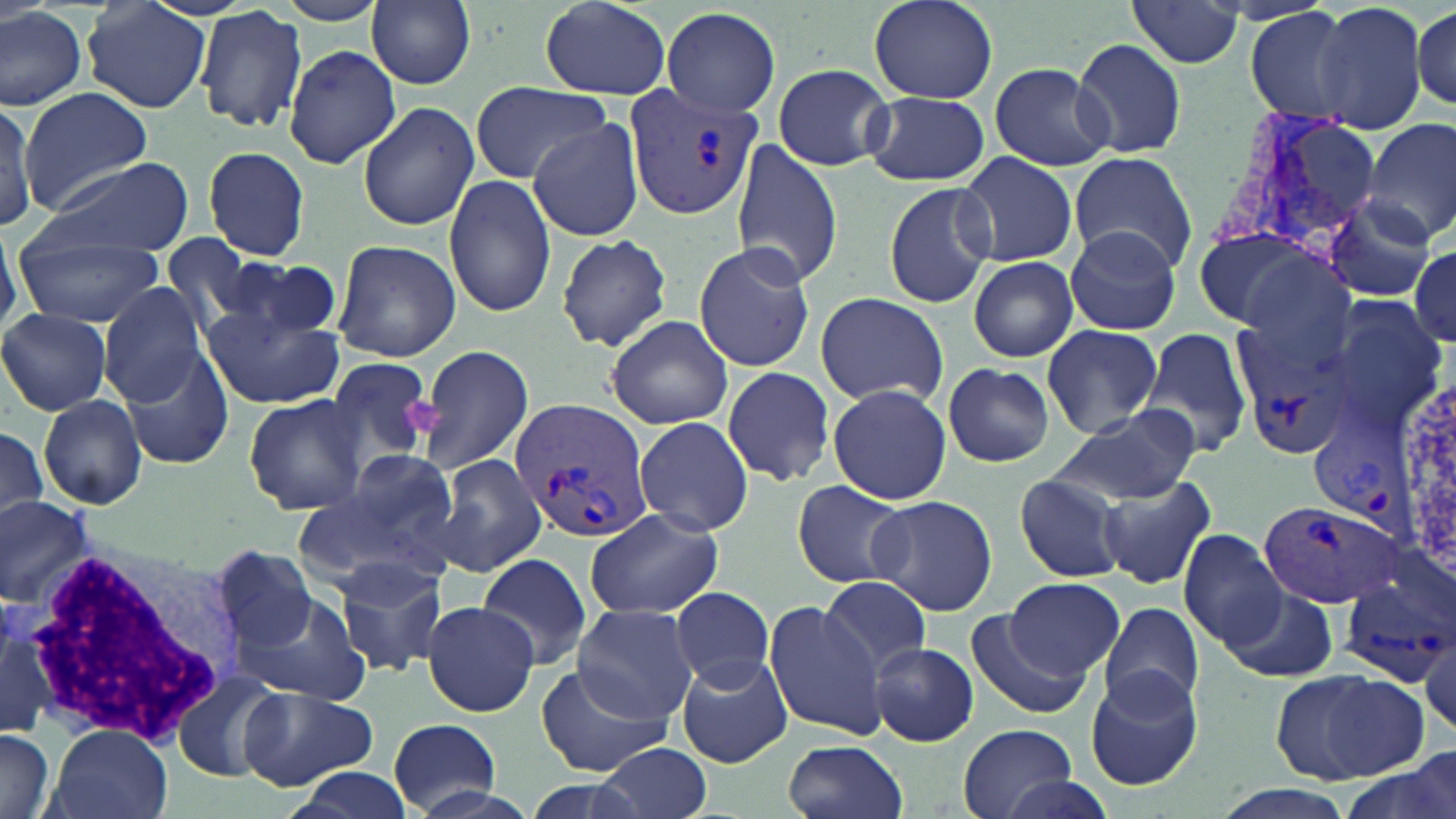

Summary:
  - Coordinate format: approximate bounding boxes as (x1,y1)-(x2,y2) corner pairs in pixels
  - White blood cell locations: (21,534)-(247,748)
  - Uninfected red blood cell locations: (366,0)-(476,89), (540,0)-(671,97), (870,0)-(997,104), (1125,0)-(1244,72), (82,1)-(212,114), (1312,1)-(1429,134), (1,5)-(86,111), (195,5)-(308,135), (1414,5)-(1454,111), (660,6)-(781,117), (1244,6)-(1358,124), (1069,37)-(1188,160), (284,44)-(402,170), (773,62)-(892,171), (988,63)-(1113,171), (468,80)-(615,184), (20,88)-(152,213), (863,91)-(989,186), (358,100)-(479,231), (0,101)-(35,234), (1363,117)-(1456,244), (527,118)-(647,242), (731,141)-(843,287), (203,144)-(311,261), (954,150)-(1078,267), (1068,152)-(1198,275), (38,156)-(192,259), (445,173)-(556,319), (883,181)-(995,309), (1324,196)-(1439,302), (1064,225)-(1181,336), (16,229)-(164,327), (1185,229)-(1313,329), (555,233)-(672,353), (160,236)-(263,336), (332,239)-(460,362), (693,242)-(815,373), (1411,245)-(1455,343), (1232,250)-(1357,381), (222,255)-(346,345), (967,256)-(1080,363), (99,283)-(209,408), (813,292)-(950,408), (1323,297)-(1449,432), (203,303)-(344,411), (0,308)-(112,415), (605,315)-(734,429), (1040,325)-(1165,440), (1137,326)-(1253,461), (415,344)-(534,477), (123,352)-(231,470), (322,357)-(436,464), (941,362)-(1055,467), (720,364)-(837,487), (826,384)-(952,504), (243,393)-(368,515), (40,394)-(148,510), (1052,405)-(1202,507), (633,416)-(754,537), (0,417)-(53,524), (311,449)-(463,576), (433,454)-(549,577), (1012,472)-(1129,584), (1098,477)-(1216,589), (791,479)-(914,590), (867,495)-(997,615), (1,497)-(95,607), (585,509)-(725,623), (1177,529)-(1283,649), (218,545)-(318,651), (477,552)-(593,671), (332,555)-(448,675), (820,574)-(934,678), (1004,578)-(1125,677), (670,586)-(774,687), (231,588)-(373,704), (1222,588)-(1338,683), (422,599)-(540,716), (764,601)-(886,740), (1100,601)-(1204,713), (574,604)-(699,723), (0,605)-(64,740), (963,610)-(1090,722), (1417,628)-(1455,742), (869,642)-(978,746), (676,654)-(793,767), (536,662)-(674,777), (177,668)-(285,780), (1085,668)-(1204,792), (1281,669)-(1428,783), (239,685)-(378,792), (387,716)-(499,815), (958,723)-(1077,819), (0,725)-(55,819), (44,726)-(173,819), (783,739)-(907,819), (596,741)-(712,819), (288,766)-(419,819), (991,773)-(1120,819), (1206,786)-(1362,819)
  - Platelet locations: (398,395)-(446,438)
  - Plasmodium vivax-infected red blood cell locations: (622,85)-(763,222), (1215,104)-(1379,258), (1233,318)-(1358,466), (510,397)-(654,545), (1309,423)-(1423,548), (1258,498)-(1402,609), (1338,561)-(1454,687)
  - Slide-level diagnosis: Plasmodium vivax
  - Magnification: 1000x
  - Image size: 1456×819 pixels
  - Modality: light microscopy
  - Stain: May-Grünwald-Giemsa
  - Field of view: one of a larger specimen
  - Preparation: thin blood film